Report the malaria status of this cell.
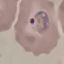
It is parasitized.

Summary:
  - Capture: smartphone camera at the microscope eyepiece
  - Preparation: thin blood film
  - Stain: Giemsa
  - Image type: cell patch, automatically extracted from a larger field of view and resized to 64 × 64 pixels